Report the malaria status of this cell.
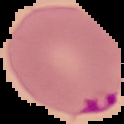
It is parasitized.

Summary:
  - Preparation: thin blood film
  - Image type: segmented cell region on a black background
  - Image size: 124×124 pixels